Outline each P. falciparum parasite and classify it by life-cycle stage.
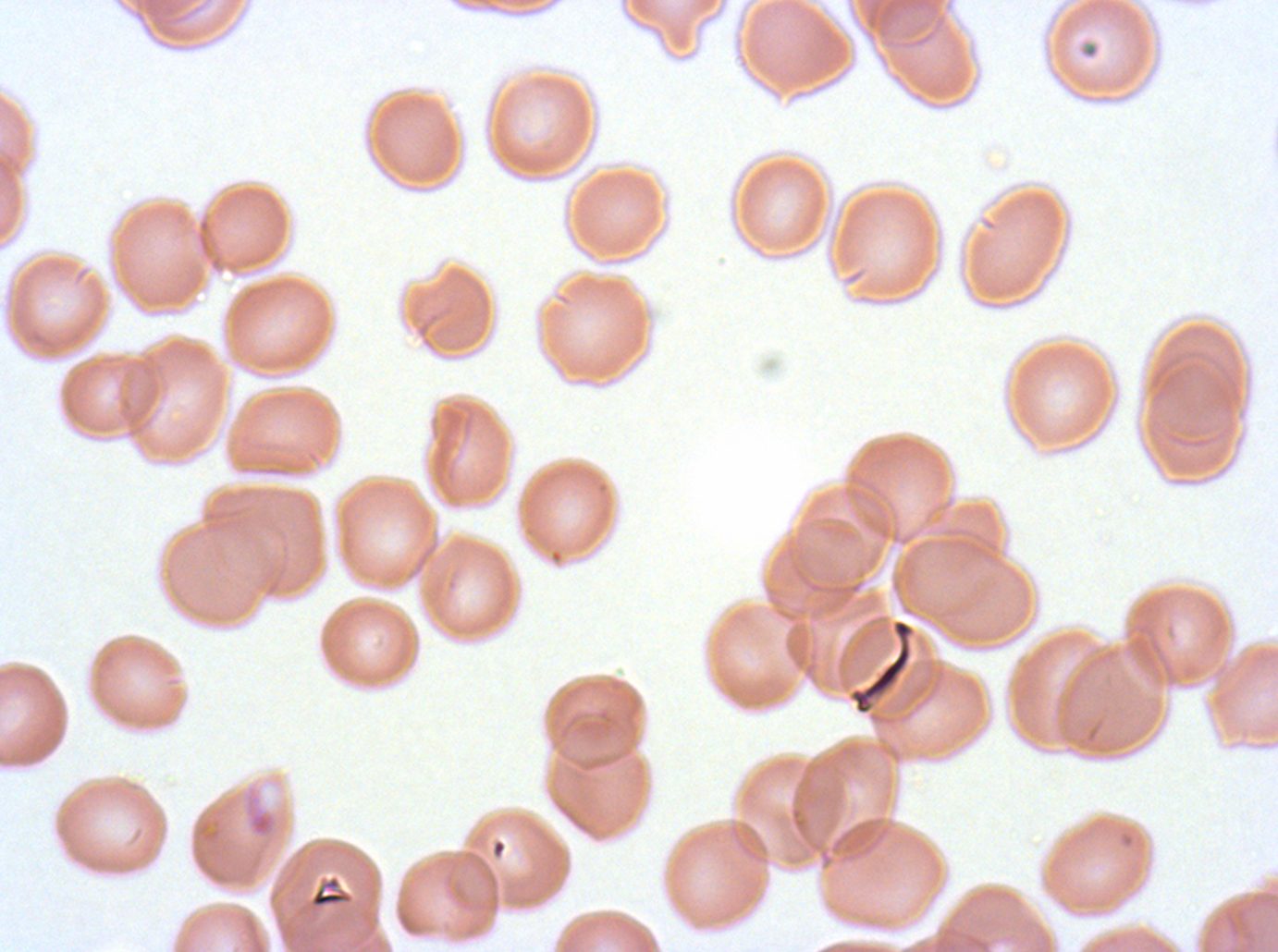
Approximate bounding boxes as [x1, y1, x2, y2] in pixels.
Rings: [245, 799, 277, 838].
No late-ring/early-trophozoite forms, mid trophozoites, late trophozoites, early schizonts, late schizonts, segmenters, or gametocytes observed.

Summary:
  - Debris locations: [1077, 41, 1100, 60], [850, 618, 913, 714], [308, 874, 354, 909]
  - Image size: 1278×952 pixels
  - Specimen: ex-vivo P. falciparum culture from a patient in The Gambia, grown for 24 to 48 hours
  - Preparation: thin blood film
  - Stain: Giemsa
  - Field of view: one sub-image of a larger composite